Give the position of every Plasmodium parasite.
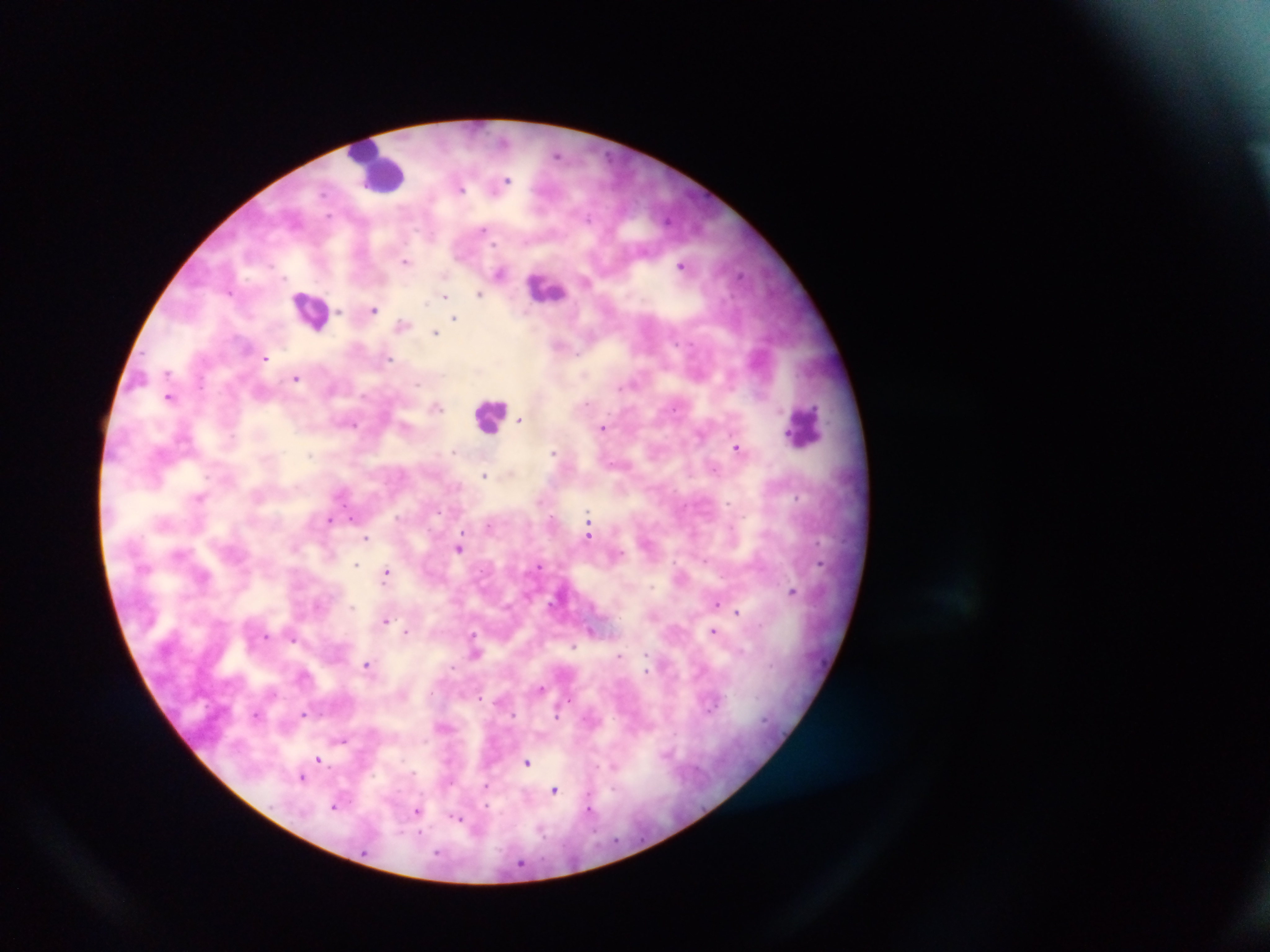
Approximate centers as (x, y) in pixels.
Plasmodium parasites: (503, 141), (556, 154), (507, 180), (460, 188), (589, 218), (483, 228), (405, 261), (681, 266), (500, 272), (741, 274), (285, 278), (585, 281), (479, 294), (445, 296), (373, 309), (339, 312), (454, 318), (403, 325), (435, 332), (676, 342), (265, 359), (389, 359), (167, 372), (296, 378), (418, 384), (620, 386), (169, 397), (587, 402), (437, 407), (675, 408), (521, 419), (354, 425), (603, 427), (232, 436), (736, 447), (453, 451), (553, 453), (311, 455), (484, 475), (199, 497), (797, 497), (728, 503), (588, 517), (351, 518), (330, 520), (489, 526), (462, 534), (589, 536), (366, 538), (459, 548), (620, 552), (705, 561), (820, 563), (355, 564), (539, 566), (387, 573), (652, 587), (792, 591), (716, 603), (352, 607), (737, 612), (386, 620), (592, 630), (406, 632), (713, 632), (474, 634), (266, 636), (293, 639), (573, 646), (475, 653), (619, 656), (647, 657), (367, 664), (646, 668), (541, 688), (304, 713), (257, 714), (557, 716), (341, 740), (319, 759), (527, 762), (613, 765), (302, 777), (485, 785), (613, 789), (555, 791), (335, 806), (486, 807), (589, 808), (416, 813), (456, 818).

Leukocyte locations: (377, 167), (547, 288), (310, 309), (490, 415), (804, 426). Sample from Ghana. Image is 1270×952 pixels. Thick blood smear. Photographed through a microscope with a mobile-phone camera. One field of view.